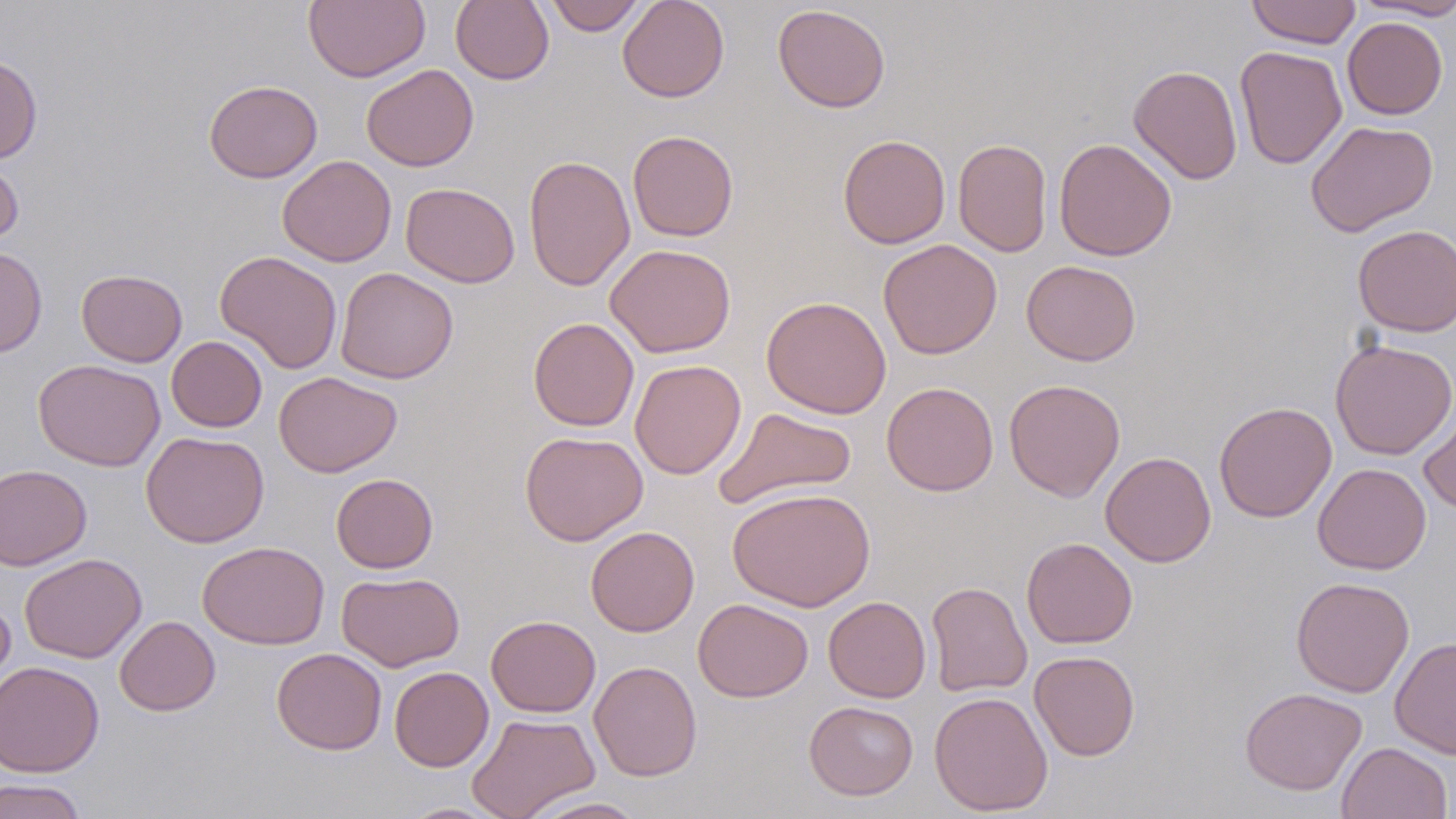

Summary:
  - Coordinate format: approximate bounding boxes as (x1,y1)-(x2,y2) corner pairs in pixels
  - Uninfected red blood cell locations: (304,0)-(430,83), (451,0)-(554,85), (543,0)-(646,35), (617,0)-(729,102), (1246,0)-(1361,48), (1355,0)-(1456,20), (772,4)-(891,113), (1342,17)-(1448,120), (1234,46)-(1347,169), (0,55)-(42,163), (361,64)-(479,171), (1128,64)-(1243,185), (204,80)-(322,183), (1305,120)-(1438,236), (627,130)-(739,242), (837,134)-(951,249), (953,138)-(1053,256), (1053,138)-(1177,261), (0,154)-(24,251), (523,154)-(635,292), (277,155)-(396,267), (400,182)-(520,288), (1352,224)-(1456,337), (878,238)-(1002,359), (605,243)-(736,358), (0,246)-(48,358), (215,250)-(343,374), (1022,259)-(1141,365), (335,267)-(458,384), (76,269)-(187,367), (761,295)-(892,418), (527,317)-(639,431), (166,336)-(267,432), (1329,339)-(1456,460), (33,358)-(166,471), (629,359)-(746,479), (274,371)-(402,478), (1004,378)-(1126,502), (881,381)-(999,496), (1214,402)-(1337,523), (1419,403)-(1456,515), (714,406)-(857,510), (140,430)-(269,548), (520,430)-(648,546), (1100,450)-(1216,568), (1312,463)-(1431,574), (0,464)-(92,571), (331,473)-(438,573), (727,486)-(876,611), (585,526)-(699,637), (1021,537)-(1138,649), (197,541)-(330,650), (19,553)-(147,663), (337,571)-(464,672), (1290,577)-(1415,697), (926,581)-(1032,697), (0,593)-(16,696), (823,595)-(931,703), (692,598)-(813,702), (115,615)-(220,716), (486,615)-(601,717), (1390,636)-(1456,759), (271,648)-(387,755), (1028,650)-(1141,761), (0,660)-(105,778), (589,660)-(702,782), (389,666)-(494,772), (1239,687)-(1368,796), (928,690)-(1053,816), (804,700)-(919,801), (466,712)-(600,819), (1337,741)-(1453,819), (0,777)-(89,819), (521,796)-(650,818), (398,802)-(506,818)
  - Slide-level diagnosis: negative for blood parasites
  - Stain: May-Grünwald-Giemsa
  - Preparation: thin blood smear
  - Field of view: one of a larger specimen
  - Modality: optical microscopy
  - Magnification: 1000x
  - Image size: 1456×819 pixels